Report the malaria status of this cell.
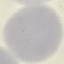
It is uninfected.

Summary:
  - Stain: Giemsa
  - Capture: smartphone through the microscope eyepiece
  - Preparation: thin blood smear
  - Image type: automatically extracted cell patch, resized to 64 × 64 pixels